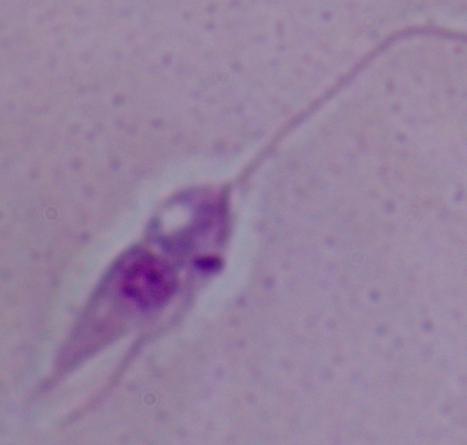
A Leishmania parasite is shown. Captured at 1000x magnification. Photomicrograph.